Identify the parasite.
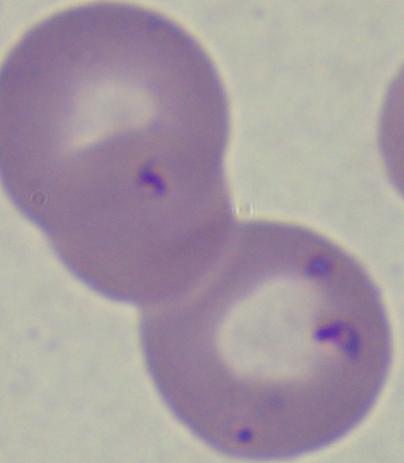
Babesia.

Summary:
  - Modality: micrograph
  - Magnification: 1000x